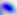
Summary:
  - Identification: Toxoplasma gondii
  - Modality: micrograph
  - Magnification: 400x